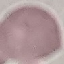
Result: negative for malaria parasites. Thin smear of blood. Giemsa-stained preparation. Photographed with a smartphone camera at the microscope eyepiece. Automatically extracted cell patch, resized to 64 × 64 pixels.